Give the position of every Plasmodium parasite.
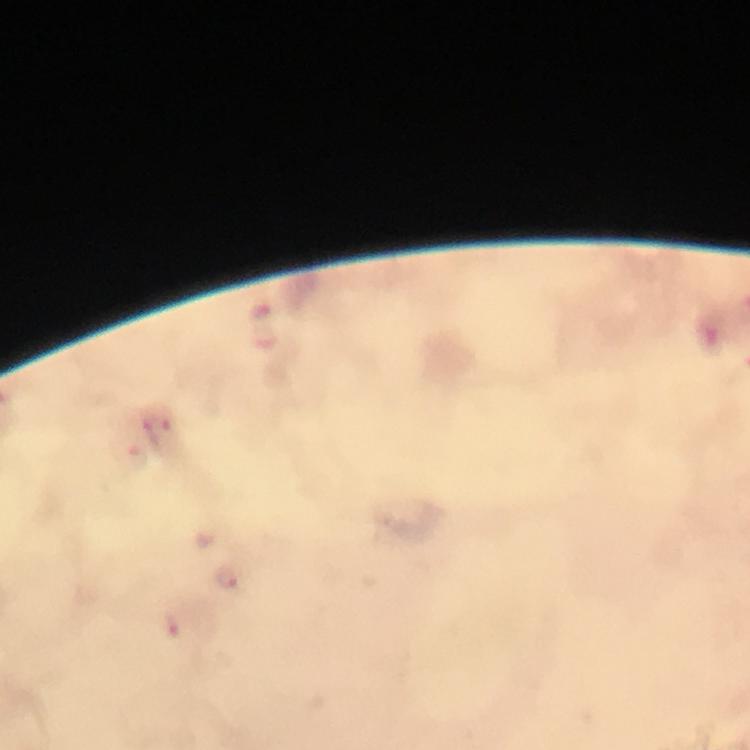
Approximate centers as {x, y} in pixels.
Plasmodium parasites: {262, 314}, {138, 457}, {226, 576}, {176, 625}.

Giemsa stain. Smartphone photograph taken through a microscope. Thick blood film. From a malaria diagnostic workup. 100x magnification. Immersion oil applied. A crop from one field of view. Image is 750×750 pixels.